Classify this cell by malaria status.
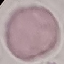
Uninfected.

capture = smartphone through the microscope eyepiece
preparation = thin smear
image type = automatically extracted cell patch, resized to 64 × 64 pixels
stain = Giemsa